Locate every blood parasite and identify its species.
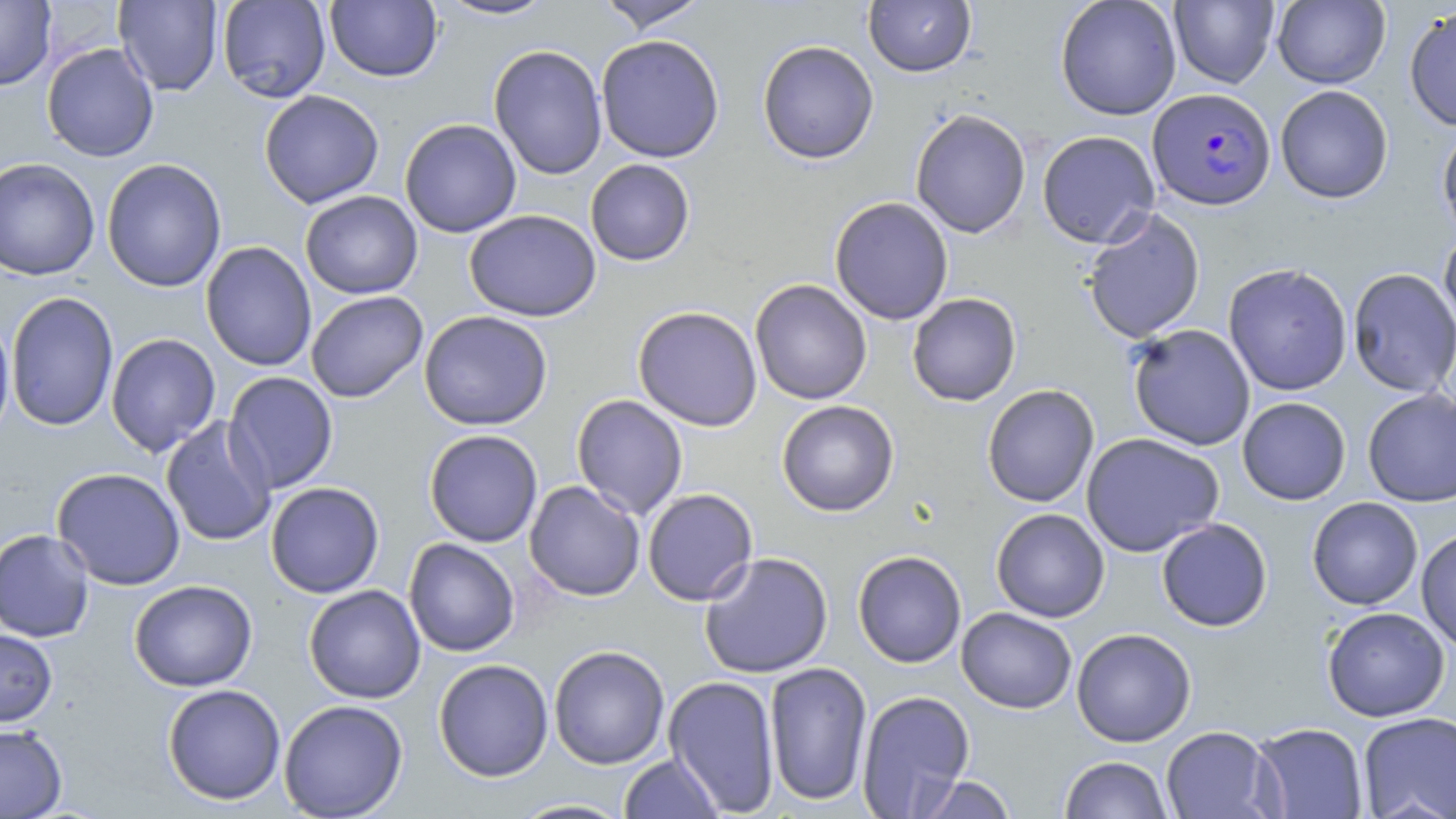
Approximate bounding boxes as (x1, y1, x2, y2) in pixels.
Plasmodium falciparum-infected red blood cells: (1147, 87, 1276, 211).
No Plasmodium ovale, Plasmodium malariae, Plasmodium vivax, Babesia divergens, or Trypanosoma brucei observed.

Uninfected red blood cell locations: (0, 0, 56, 90), (218, 0, 331, 103), (325, 0, 443, 83), (434, 0, 560, 21), (595, 0, 711, 34), (863, 0, 976, 77), (1055, 0, 1182, 120), (1272, 0, 1390, 88), (114, 1, 223, 96), (1169, 1, 1279, 88), (1404, 6, 1456, 132), (595, 35, 725, 163), (756, 40, 879, 164), (42, 43, 159, 162), (488, 45, 608, 180), (1275, 85, 1394, 204), (259, 89, 384, 209), (910, 108, 1032, 239), (399, 118, 522, 238), (1437, 122, 1456, 244), (1036, 130, 1161, 248), (0, 156, 100, 281), (102, 158, 227, 293), (585, 159, 695, 266), (300, 190, 423, 299), (829, 196, 954, 325), (1081, 208, 1206, 344), (464, 209, 601, 322), (1439, 229, 1456, 338), (200, 241, 317, 372), (1223, 263, 1353, 396), (1348, 267, 1456, 398), (750, 279, 872, 405), (6, 291, 119, 432), (305, 291, 428, 403), (907, 292, 1022, 406), (632, 305, 763, 431), (0, 309, 14, 448), (419, 310, 553, 431), (1128, 324, 1256, 451), (105, 333, 221, 457), (223, 371, 339, 494), (982, 384, 1099, 508), (1362, 388, 1456, 506), (571, 394, 688, 519), (1237, 397, 1351, 505), (776, 400, 899, 517), (160, 416, 276, 548), (424, 429, 543, 548), (1080, 432, 1224, 557), (51, 467, 186, 590), (524, 480, 645, 601), (265, 482, 384, 598), (642, 488, 758, 606), (1307, 497, 1423, 610), (991, 508, 1110, 623), (1156, 518, 1273, 632), (0, 528, 95, 643), (1415, 528, 1456, 652), (404, 538, 520, 657), (852, 550, 967, 668), (699, 551, 834, 678), (129, 579, 257, 692), (304, 585, 426, 704), (1322, 606, 1450, 722), (956, 607, 1077, 714), (0, 628, 57, 726), (1071, 628, 1197, 747), (549, 645, 670, 770), (433, 659, 554, 782), (764, 661, 873, 807), (663, 675, 781, 814), (162, 683, 286, 805), (856, 690, 976, 816), (278, 699, 408, 818), (1357, 711, 1456, 819), (1250, 722, 1369, 819), (0, 724, 67, 819), (1161, 726, 1281, 819), (618, 753, 725, 819), (1059, 755, 1173, 818), (908, 773, 1020, 818), (508, 798, 634, 818). Slide-level diagnosis: Plasmodium falciparum. Optical microscopy. 1000x magnification. Thin blood film. One field of a larger specimen. May-Grünwald-Giemsa stain. Image is 1456×819 pixels.